Report the malaria status of this cell.
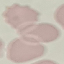

It is uninfected.

Thin smear of blood. Giemsa-stained preparation. Acquired by smartphone through the microscope eyepiece. Cell patch, automatically extracted from a larger field of view and resized to 64 × 64 pixels.